Assess this cell for malaria.
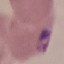

It is parasitized.

{
  "capture": "smartphone camera at the microscope eyepiece",
  "stain": "Giemsa",
  "preparation": "thin smear",
  "image_type": "cell patch, automatically extracted from a larger field of view and resized to 64 × 64 pixels"
}